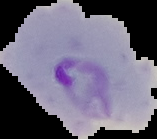

result = Plasmodium parasites identified
image type = segmented cell region with the area outside set to black
preparation = thin blood film
image size = 157×139 pixels